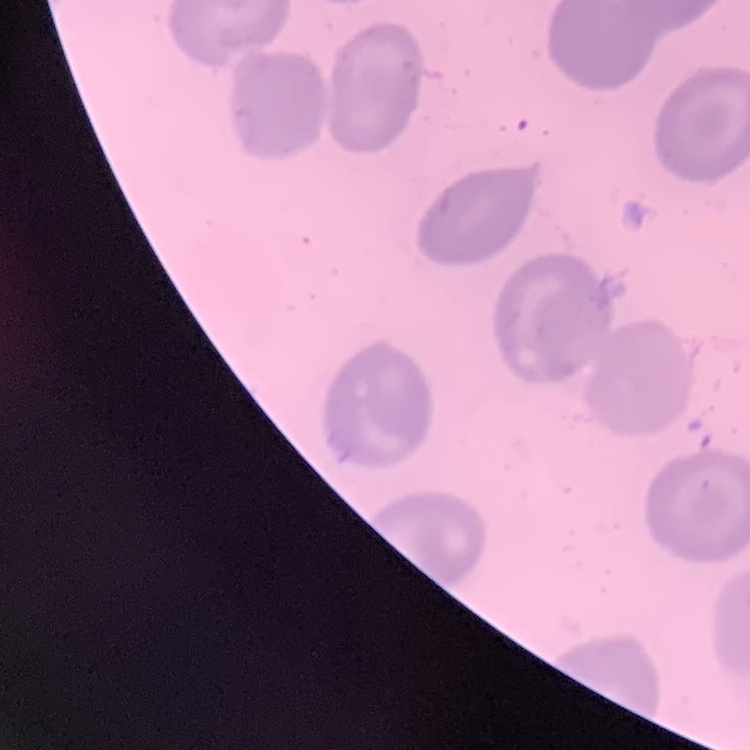
The red blood cells exhibit no rouleaux formation. Square crop of a larger photomicrograph. Thin peripheral smear. Stained with either Field's or Giemsa.